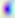 Captured at 400x magnification. Toxoplasma gondii is seen. Photomicrograph.